Locate every blood parasite and identify its species.
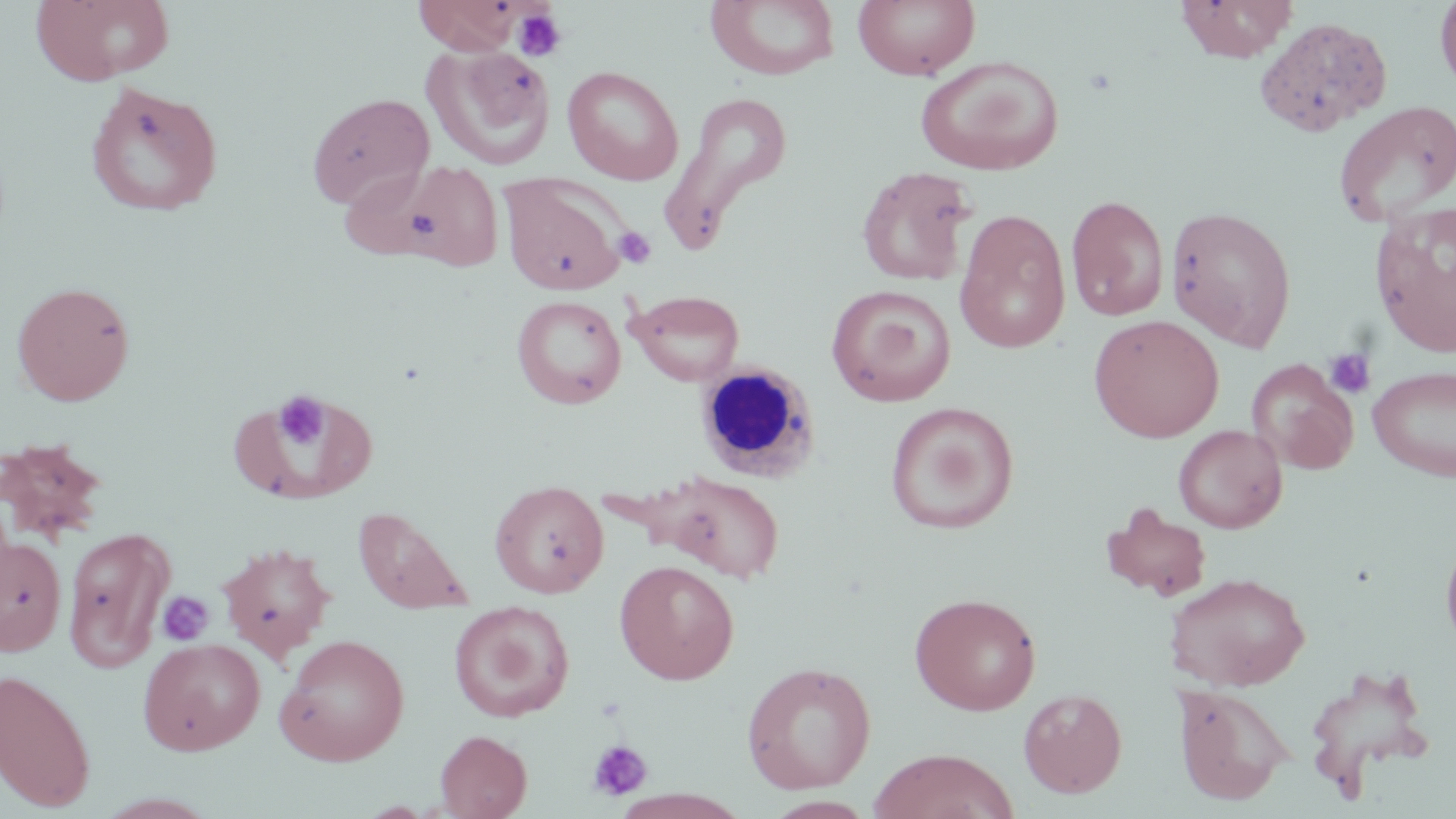

No blood parasites seen.

Summary:
  - Coordinate format: approximate bounding boxes as (x1,y1)-(x2,y2) corner pairs in pixels
  - White blood cell locations: (694,361)-(821,482)
  - Platelet locations: (513,8)-(567,62), (613,226)-(656,268), (1323,347)-(1377,400), (272,392)-(330,452), (156,591)-(215,647), (587,739)-(653,801)
  - Uninfected red blood cell locations: (31,0)-(176,85), (413,0)-(526,56), (853,0)-(980,80), (1176,0)-(1298,62), (1435,0)-(1456,96), (705,1)-(841,81), (426,45)-(556,170), (916,55)-(1064,176), (562,66)-(684,185), (85,80)-(224,217), (660,90)-(794,251), (306,92)-(434,210), (1332,101)-(1456,228), (352,158)-(506,270), (857,166)-(976,286), (499,173)-(628,296), (1066,195)-(1169,322), (1371,203)-(1456,356), (1166,206)-(1297,350), (954,209)-(1071,354), (11,280)-(135,406), (827,284)-(956,407), (626,289)-(745,386), (511,294)-(627,409), (1088,314)-(1225,442), (1247,359)-(1359,474), (1368,365)-(1456,483), (885,401)-(1019,534), (1173,425)-(1287,533), (0,437)-(109,544), (651,471)-(785,583), (490,480)-(609,598), (1101,503)-(1213,601), (352,505)-(474,613), (62,524)-(173,673), (1440,529)-(1456,656), (0,534)-(66,655), (215,542)-(337,660), (614,560)-(739,684), (1164,571)-(1310,691), (909,592)-(1042,716), (448,601)-(575,722), (275,633)-(410,766), (137,637)-(266,755), (740,661)-(877,794), (1303,665)-(1436,799), (0,668)-(96,812), (1173,682)-(1294,806), (1018,688)-(1127,797), (435,730)-(532,818), (868,748)-(1020,819)
  - Slide-level diagnosis: no evidence of blood parasites
  - Magnification: 1000x
  - Field of view: one of a larger specimen
  - Stain: May-Grünwald-Giemsa
  - Modality: optical microscopy
  - Image size: 1456×819 pixels
  - Preparation: thin blood smear